Name the parasite shown.
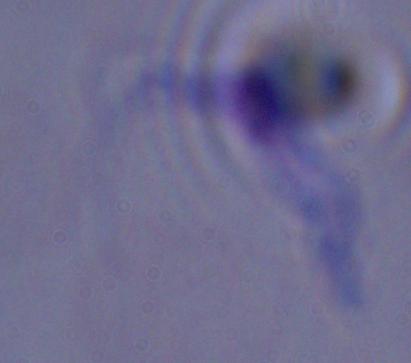

A trypanosome.

modality = micrograph
magnification = 1000x